Assess the morphology of the red blood cells.
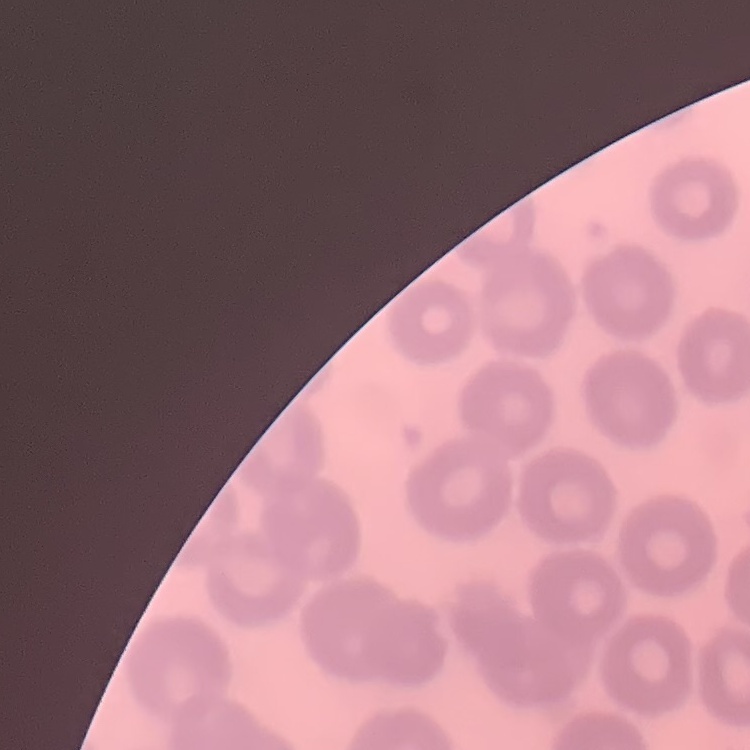
No rouleaux formation.

stain = Field's or Giemsa
image type = one tile cut from a larger photomicrograph
preparation = thin blood film